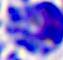

modality = photomicrograph
magnification = 400x
identification = white blood cell